Assess the morphology of the erythrocytes.
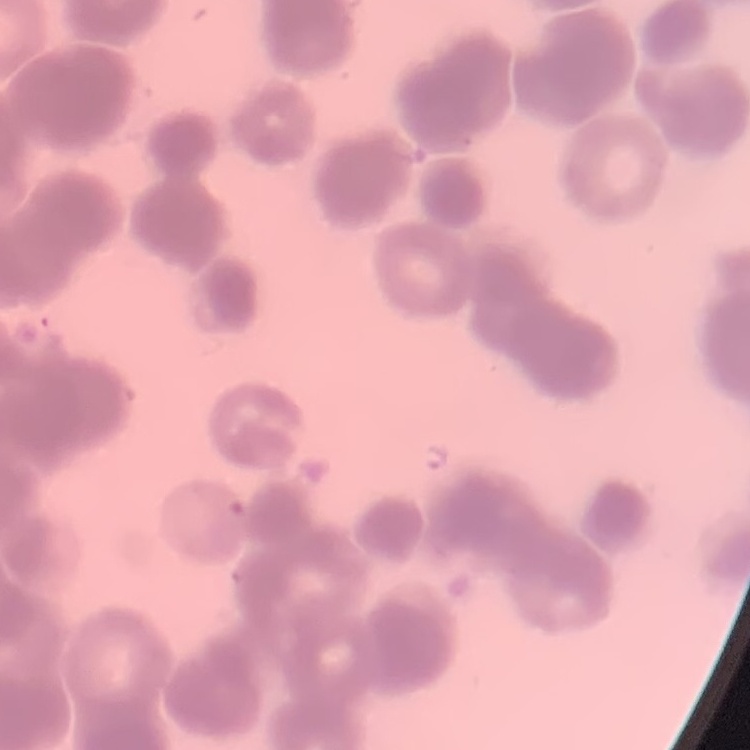

They show rouleaux formation.

Summary:
  - Image type: square crop of a larger photomicrograph
  - Preparation: thin blood smear
  - Stain: Field's or Giemsa